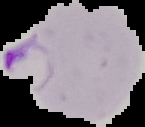

Summary:
  - Image type: segmented cell region with the area outside set to black
  - Image size: 145×127 pixels
  - Preparation: thin blood film
  - Result: malaria parasites detected